Report the malaria status of this cell.
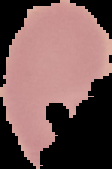
Uninfected.

Summary:
  - Preparation: thin blood smear
  - Image size: 112×169 pixels
  - Image type: segmented cell region with the area outside set to black